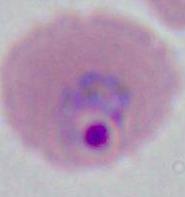 A Plasmodium parasite is shown. Photomicrograph. Captured at either 400x or 1000x magnification.